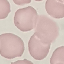

Result: no malaria parasites seen. Thin blood film. Photographed with a smartphone camera at the microscope eyepiece. Cell patch, automatically extracted from a larger field of view and resized to 64 × 64 pixels. Giemsa stain.